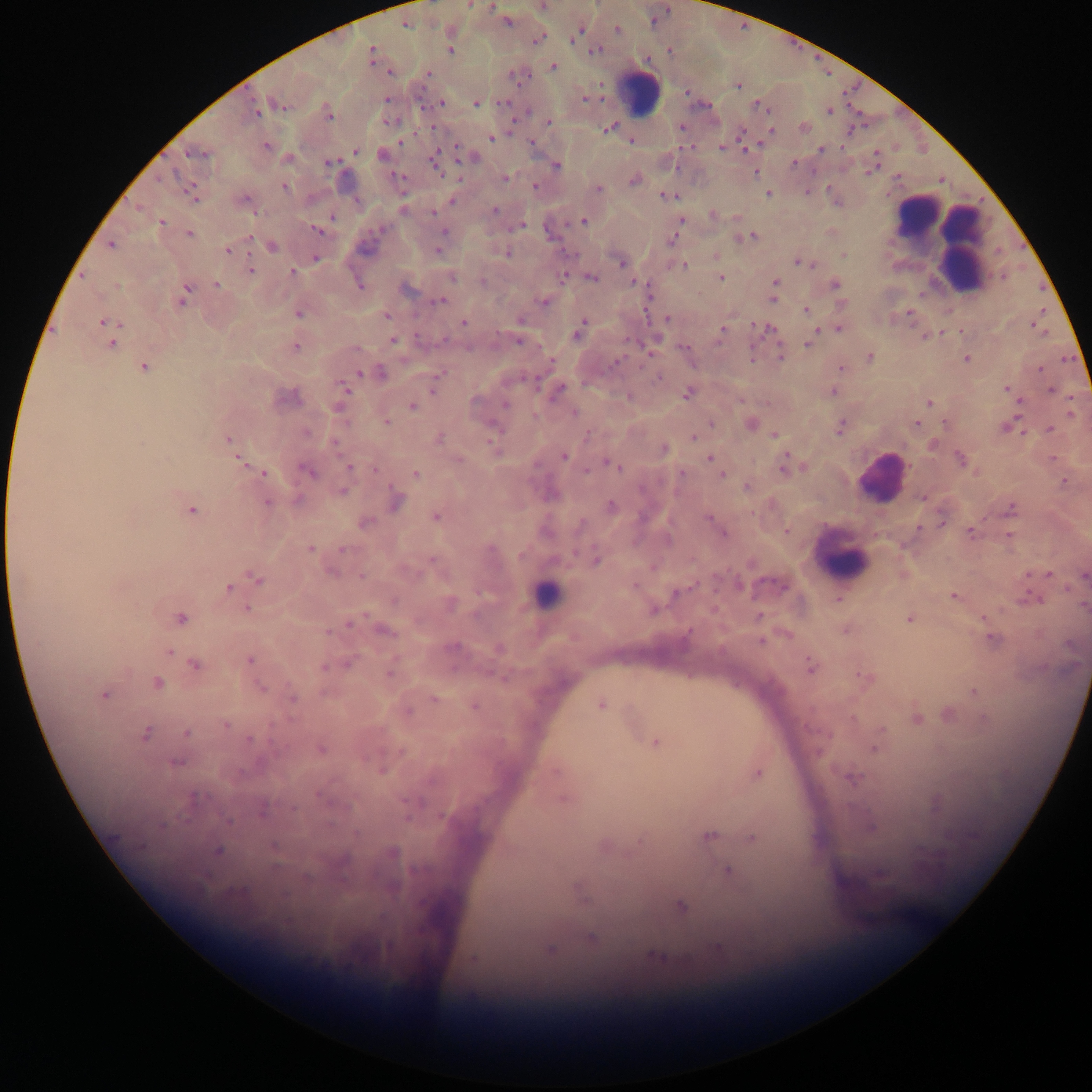
Approximate centers as {x, y} in pixels.
Summary:
  - Malaria parasite locations: {469, 5}, {543, 6}, {507, 21}, {405, 23}, {618, 30}, {580, 31}, {537, 39}, {450, 50}, {595, 50}, {371, 54}, {553, 66}, {391, 72}, {428, 73}, {515, 74}, {738, 85}, {583, 98}, {441, 102}, {475, 103}, {279, 104}, {757, 105}, {254, 110}, {829, 110}, {328, 113}, {548, 121}, {681, 127}, {609, 128}, {804, 128}, {770, 130}, {742, 136}, {492, 137}, {631, 141}, {531, 142}, {744, 146}, {266, 147}, {722, 147}, {822, 149}, {355, 150}, {196, 152}, {383, 155}, {472, 157}, {435, 158}, {330, 162}, {794, 162}, {556, 166}, {872, 168}, {755, 172}, {401, 178}, {506, 179}, {634, 179}, {284, 186}, {535, 186}, {597, 189}, {192, 193}, {767, 194}, {667, 196}, {452, 199}, {246, 200}, {403, 208}, {494, 210}, {433, 213}, {713, 215}, {736, 216}, {332, 217}, {582, 221}, {679, 221}, {162, 222}, {519, 225}, {318, 230}, {445, 232}, {548, 232}, {189, 233}, {676, 235}, {750, 236}, {250, 237}, {111, 245}, {272, 246}, {438, 249}, {228, 250}, {506, 252}, {842, 254}, {716, 256}, {315, 258}, {621, 261}, {799, 261}, {683, 265}, {250, 270}, {292, 272}, {563, 276}, {591, 277}, {720, 278}, {633, 281}, {774, 283}, {217, 284}, {835, 284}, {360, 286}, {406, 287}, {183, 295}, {773, 298}, {648, 300}, {438, 301}, {543, 301}, {841, 303}, {806, 309}, {298, 313}, {810, 313}, {385, 316}, {667, 318}, {521, 319}, {464, 322}, {106, 323}, {1034, 325}, {760, 327}, {579, 328}, {768, 329}, {824, 329}, {839, 329}, {722, 331}, {926, 336}, {392, 340}, {519, 341}, {111, 343}, {808, 344}, {295, 345}, {683, 347}, {780, 355}, {870, 357}, {966, 358}, {551, 360}, {143, 367}, {841, 368}, {1039, 369}, {360, 372}, {380, 372}, {659, 377}, {439, 379}, {433, 388}, {1006, 389}, {344, 390}, {558, 390}, {1051, 390}, {832, 391}, {687, 393}, {287, 396}, {628, 396}, {739, 400}, {1020, 401}, {929, 402}, {505, 404}, {339, 406}, {413, 406}, {574, 412}, {1071, 412}, {386, 422}, {711, 423}, {916, 423}, {750, 424}, {1006, 426}, {840, 427}, {1050, 429}, {588, 434}, {774, 435}, {693, 437}, {227, 438}, {438, 439}, {933, 444}, {663, 448}, {564, 456}, {709, 458}, {238, 459}, {1053, 459}, {961, 460}, {610, 464}, {784, 465}, {717, 466}, {349, 467}, {375, 469}, {308, 471}, {263, 473}, {681, 473}, {415, 474}, {721, 474}, {1065, 481}, {747, 486}, {342, 491}, {922, 497}, {394, 500}, {267, 503}, {611, 507}, {1011, 508}, {191, 509}, {435, 516}, {708, 518}, {941, 520}, {364, 522}, {786, 530}, {969, 532}, {723, 533}, {1009, 536}, {310, 549}, {343, 550}, {595, 559}, {1048, 574}, {1083, 575}, {361, 576}, {257, 579}, {738, 585}, {228, 588}, {676, 592}, {953, 595}, {1031, 596}, {838, 599}, {449, 603}, {1083, 605}, {247, 608}, {653, 609}, {760, 616}, {180, 617}, {910, 617}, {984, 618}, {350, 622}, {845, 629}, {383, 630}, {992, 638}, {760, 640}, {498, 648}, {169, 652}, {249, 660}, {347, 663}, {195, 664}, {811, 666}, {391, 670}, {865, 678}, {156, 684}, {974, 692}, {104, 693}, {292, 697}, {433, 699}, {601, 704}, {474, 705}, {407, 711}, {949, 714}, {916, 717}, {986, 718}, {225, 725}, {881, 731}, {186, 732}, {145, 733}, {656, 742}, {874, 747}, {320, 749}, {175, 761}, {382, 768}, {758, 772}, {851, 777}, {563, 797}, {936, 803}, {871, 826}, {709, 835}, {752, 837}, {218, 850}, {728, 871}, {580, 892}, {681, 906}, {592, 938}, {719, 946}, {550, 948}, {657, 955}, {473, 959}
  - Leukocyte locations: {639, 90}, {917, 213}, {963, 221}, {937, 225}, {962, 242}, {960, 270}, {881, 477}, {842, 559}, {546, 594}
  - Preparation: thick blood smear
  - Image size: 1092×1092 pixels
  - Field of view: single
  - Capture: mobile-phone photograph through a microscope
  - Country: Ghana